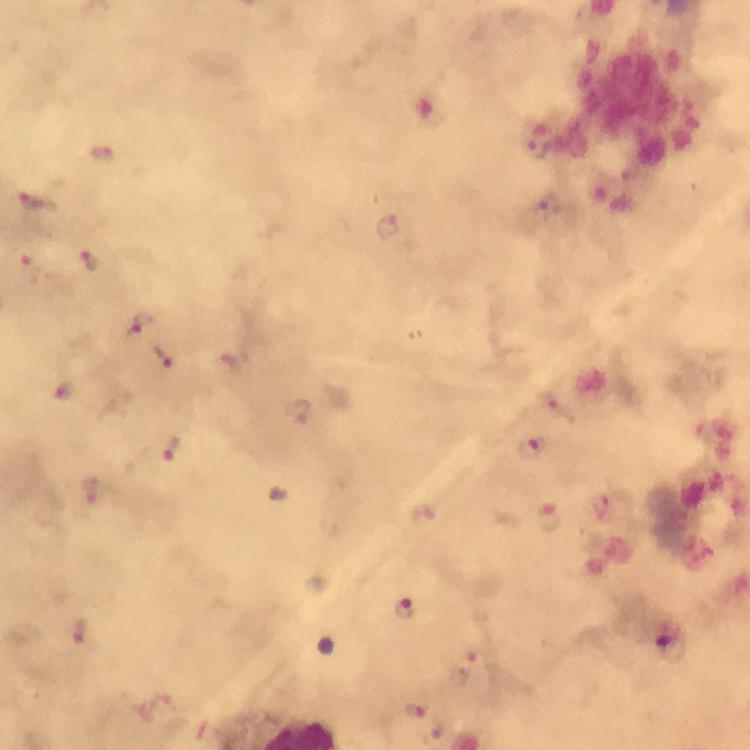

Approximate centers as (x, y) in pixels. Malaria parasite locations: (105, 154), (35, 203), (387, 225), (89, 261), (31, 267), (141, 327), (162, 356), (234, 359), (64, 391), (297, 413), (532, 447), (172, 448), (550, 516), (405, 608), (80, 631), (477, 656), (415, 711). Immersion oil was used. From a malaria diagnostic workup. Photographed through the microscope with a smartphone camera. Image is 750×750 pixels. Cropped region of a single field of view. 100x magnification. Thick blood smear. Giemsa stain.